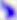
Captured at 400x magnification. Toxoplasma gondii is shown. Micrograph.